Describe the morphology of the erythrocytes.
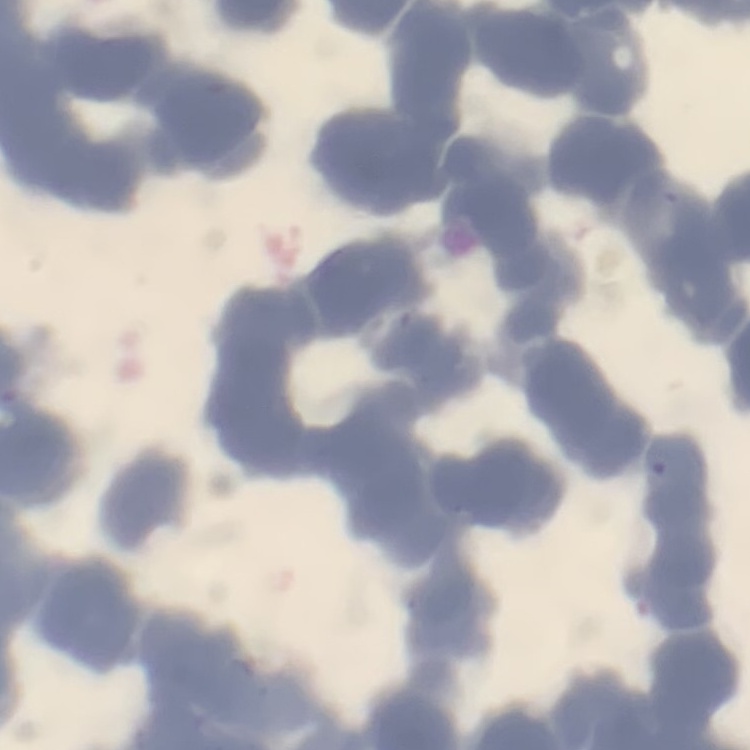
Rouleaux formation.

Summary:
  - Preparation: thin blood film
  - Image type: one tile cut from a larger photomicrograph
  - Stain: Field's or Giemsa